Report the malaria status of this cell.
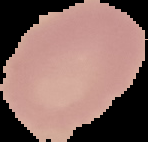
Uninfected.

{
  "preparation": "thin blood smear",
  "image_type": "segmented cell region on a black background",
  "image_size": "148×142 pixels"
}